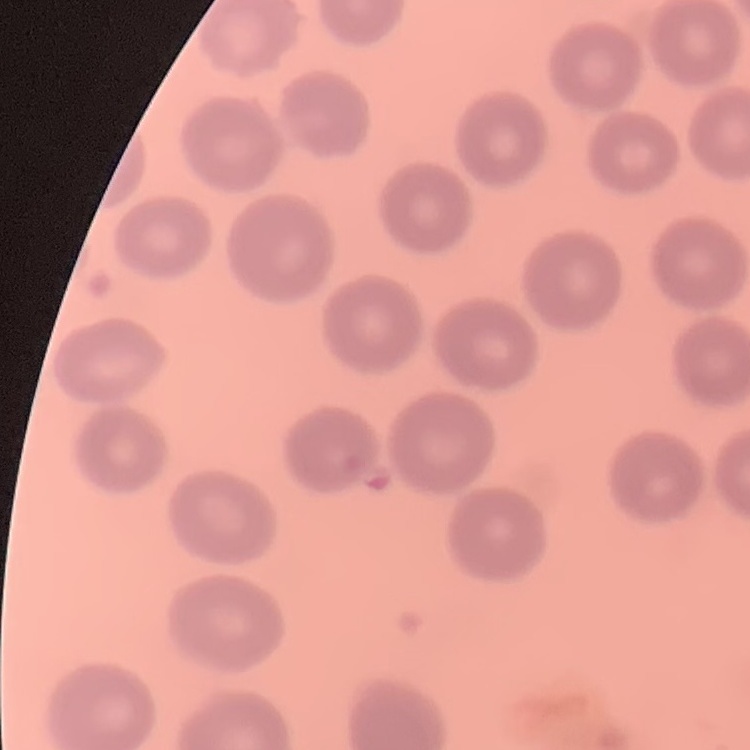
erythrocyte morphology = no rouleaux formation
image type = square crop of a larger photomicrograph
preparation = thin peripheral smear
stain = Field's or Giemsa